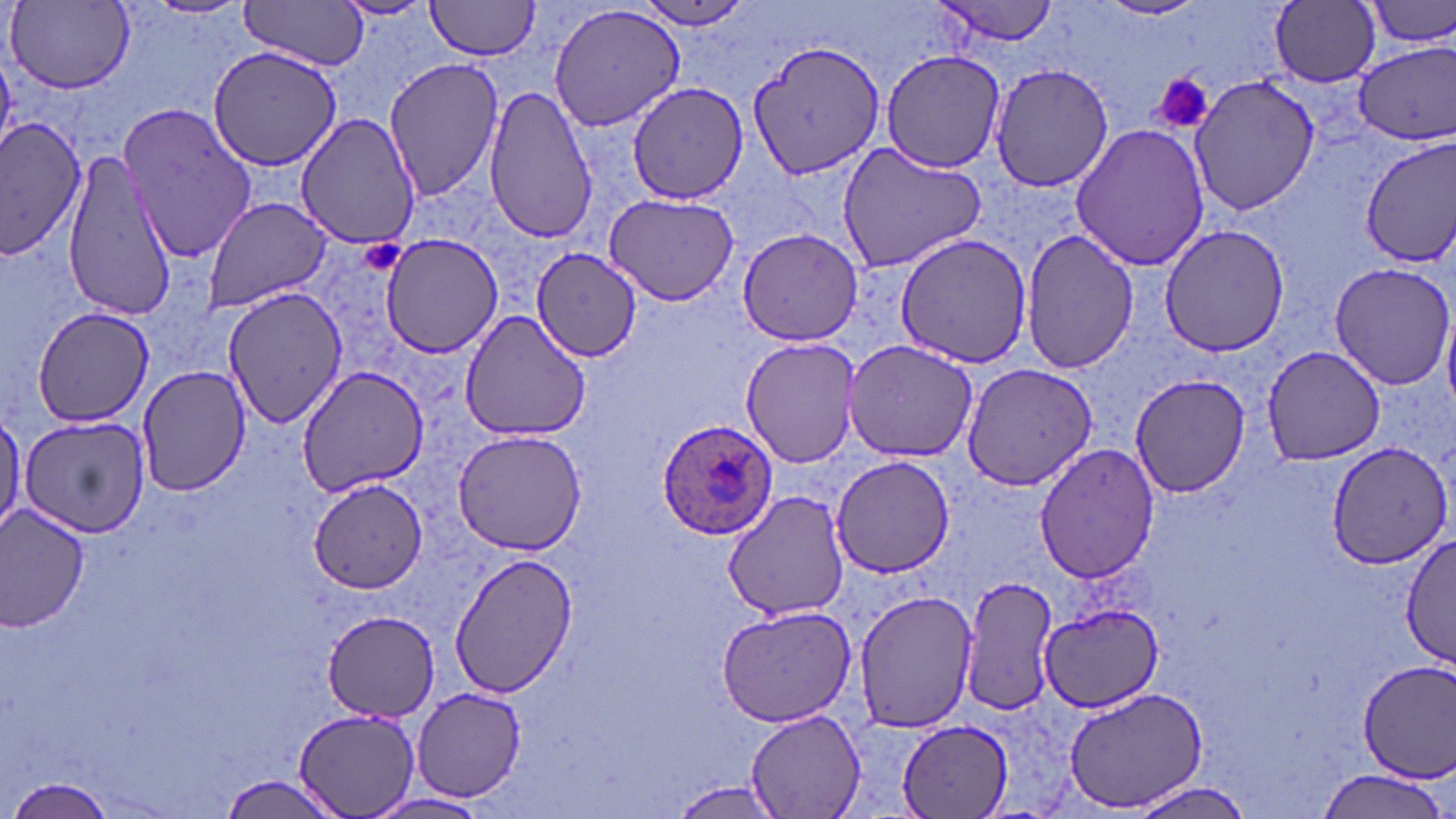
slide-level diagnosis = Plasmodium ovale
magnification = 1000x
stain = May-Grünwald-Giemsa
uninfected red blood cell locations = approximate bounding boxes as [x1, y1, x2, y2] in pixels: [330, 0, 439, 23], [424, 0, 543, 61], [930, 0, 1063, 48], [1099, 0, 1207, 22], [1366, 0, 1456, 49], [239, 1, 372, 70], [630, 1, 759, 32], [1269, 1, 1382, 88], [7, 2, 131, 93], [546, 3, 685, 133], [746, 37, 886, 180], [1351, 42, 1455, 144], [208, 44, 345, 172], [879, 50, 1006, 172], [383, 58, 506, 201], [988, 63, 1115, 194], [1189, 74, 1320, 218], [626, 81, 747, 204], [482, 85, 598, 244], [120, 103, 262, 262], [295, 112, 418, 248], [1, 115, 88, 261], [1069, 121, 1209, 273], [1360, 135, 1456, 268], [836, 144, 987, 273], [61, 150, 180, 318], [604, 193, 739, 306], [202, 197, 334, 314], [1159, 224, 1292, 358], [736, 227, 866, 347], [1021, 228, 1139, 375], [379, 233, 505, 357], [898, 234, 1032, 368], [531, 249, 643, 363], [1326, 262, 1455, 391], [223, 285, 347, 428], [31, 307, 157, 427], [460, 309, 591, 442], [741, 338, 863, 468], [842, 338, 979, 462], [1260, 344, 1388, 464], [960, 361, 1099, 491], [296, 366, 434, 497], [135, 367, 251, 497], [1127, 374, 1253, 499], [0, 405, 24, 537], [18, 414, 149, 538], [451, 427, 589, 555], [1326, 441, 1452, 570], [1034, 444, 1161, 586], [830, 456, 954, 578], [309, 482, 429, 591], [724, 490, 848, 621], [0, 503, 91, 632], [1400, 533, 1456, 673], [447, 552, 579, 698], [960, 575, 1058, 715], [852, 587, 980, 732], [1039, 601, 1164, 711], [715, 603, 856, 726], [322, 611, 440, 720], [1353, 659, 1456, 785], [410, 685, 528, 803], [1061, 685, 1210, 813], [295, 707, 422, 819], [746, 709, 865, 817], [898, 721, 1013, 817], [1314, 769, 1449, 819], [214, 775, 348, 819], [5, 776, 119, 817], [665, 781, 788, 817], [1127, 781, 1259, 819], [366, 791, 491, 817]
image size = 1456×819 pixels
platelet locations = approximate bounding boxes as [x1, y1, x2, y2] in pixels: [1152, 73, 1215, 134], [362, 238, 406, 277]
modality = light microscopy
Plasmodium ovale-infected red blood cell locations = approximate bounding boxes as [x1, y1, x2, y2] in pixels: [656, 420, 776, 540]
field of view = one of a larger specimen
preparation = thin blood smear